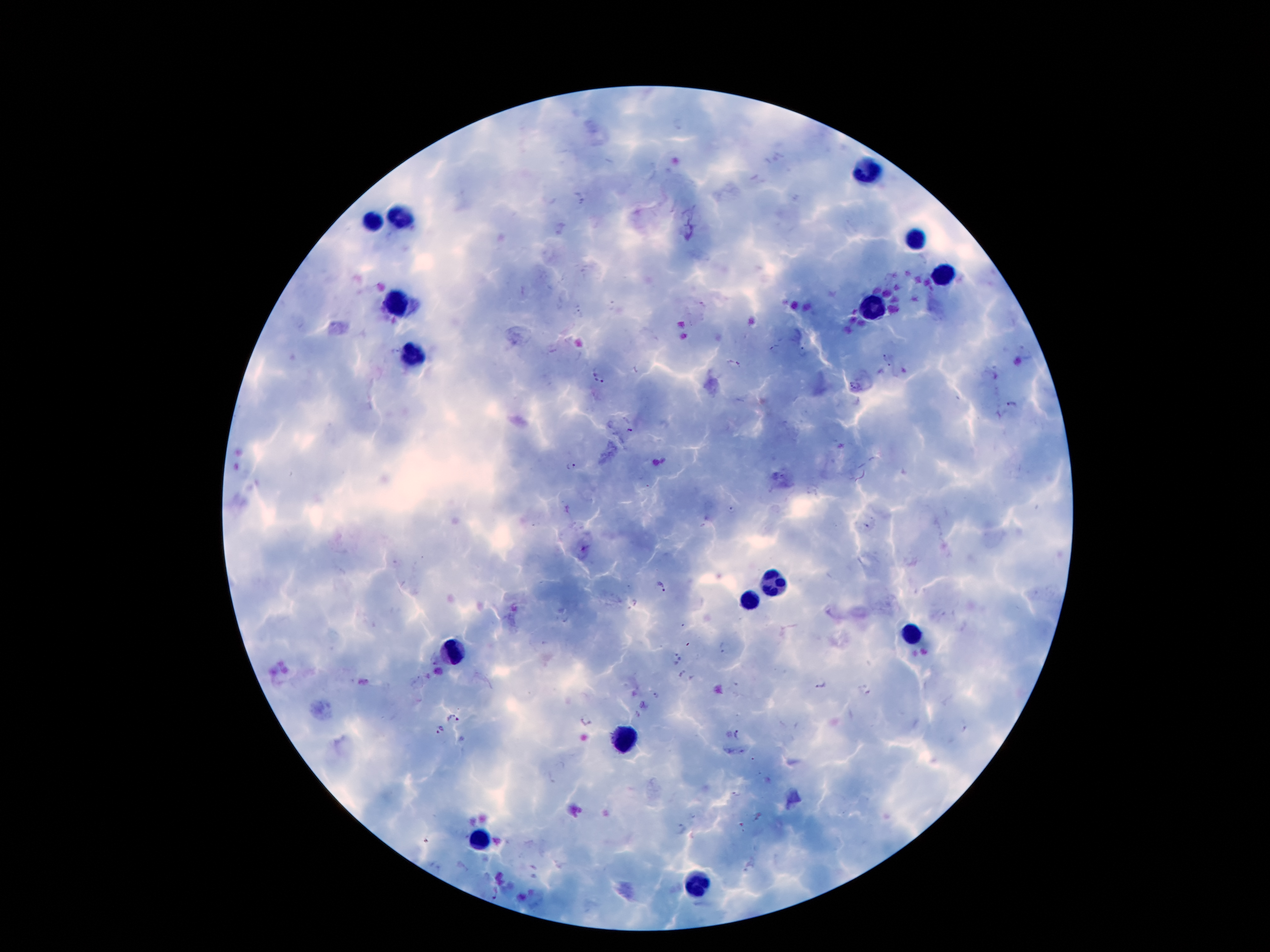
image_size: 1270×952 pixels
preparation: thick blood film
leukocyte_locations: 'approximate object centers, in pixels from the top-left corner: (x=866, y=172), (x=402, y=214), (x=373, y=219), (x=912, y=241), (x=941, y=276), (x=397, y=300), (x=870, y=309), (x=413, y=351), (x=771, y=583), (x=749, y=601), (x=912, y=634), (x=455, y=652), (x=625, y=740), (x=479, y=840), (x=696, y=886)'
malaria_parasite_locations: 'approximate object centers, in pixels from the top-left corner: (x=577, y=200), (x=578, y=314), (x=774, y=349), (x=802, y=352), (x=1026, y=352), (x=886, y=359), (x=733, y=366), (x=598, y=377), (x=1011, y=404), (x=630, y=431), (x=571, y=467), (x=733, y=510), (x=661, y=588), (x=726, y=649), (x=678, y=658), (x=435, y=659), (x=685, y=677), (x=821, y=684), (x=864, y=692), (x=656, y=697), (x=452, y=717), (x=585, y=720), (x=439, y=730), (x=741, y=735), (x=737, y=793), (x=684, y=830), (x=495, y=895)'
stain: Giemsa
patient_malaria_status: positive for Plasmodium falciparum
field_of_view: one from this slide
capture: smartphone through the microscope eyepiece
magnification: 100x